Describe the morphology of the red blood cells.
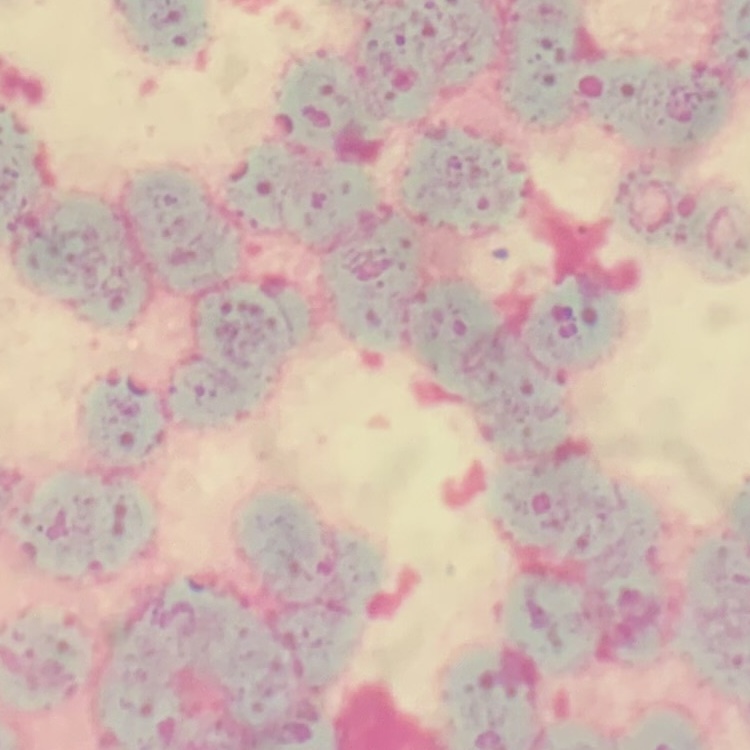

Rouleaux formation.

Summary:
  - Stain: Field's or Giemsa
  - Preparation: thin blood film
  - Image type: square crop of a larger photomicrograph